Locate and identify every blood parasite.
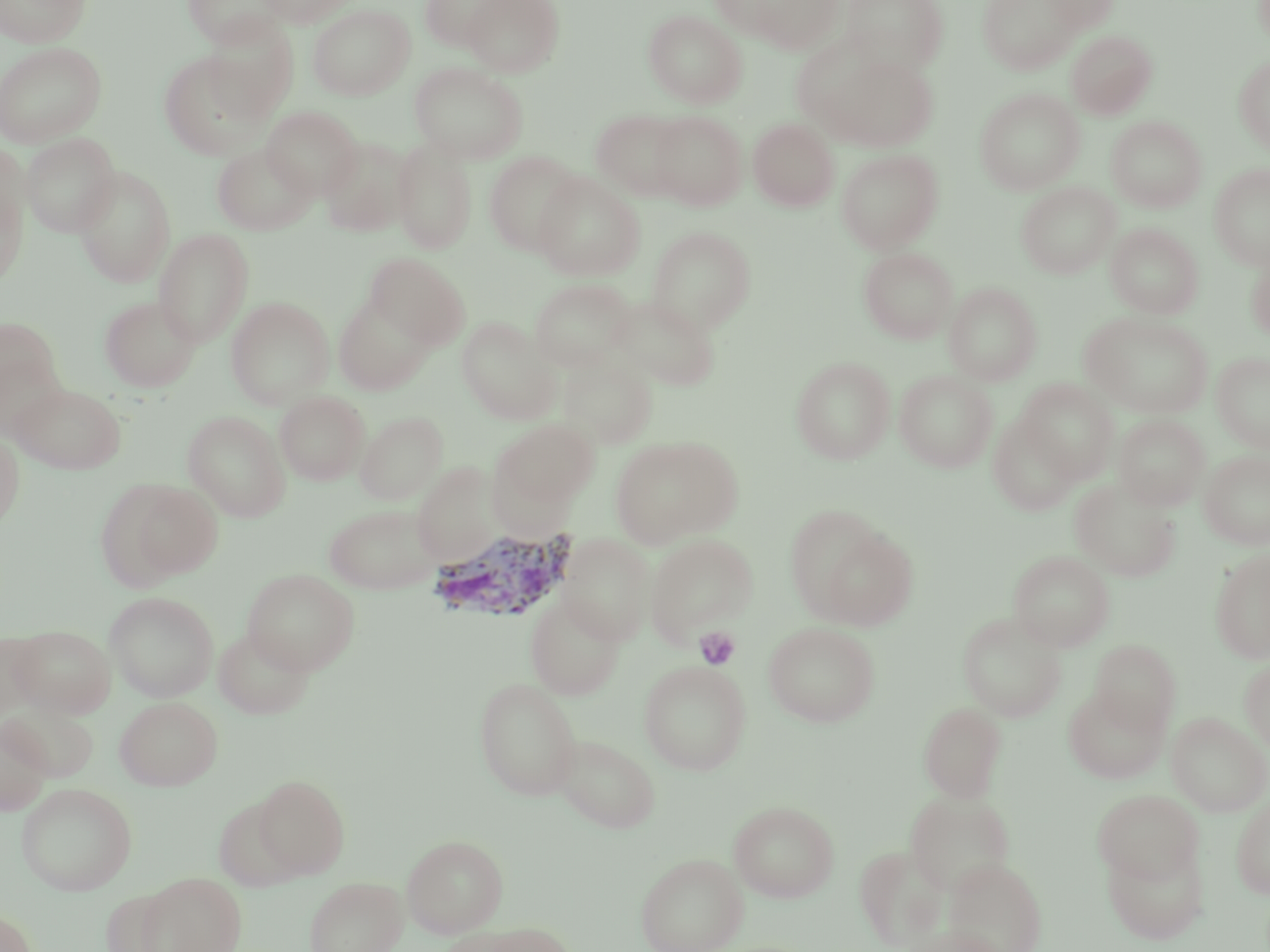

Approximate bounding boxes as named x1/y1/x2/y2 corners in pixels.
Plasmodium vivax-infected red blood cells: (x1=427, y1=528, x2=579, y2=624).
No Plasmodium falciparum, Plasmodium ovale, Plasmodium malariae, Babesia divergens, or Trypanosoma brucei observed.

Uninfected red blood cell locations: (x1=1, y1=0, x2=91, y2=47), (x1=182, y1=0, x2=286, y2=48), (x1=256, y1=0, x2=355, y2=27), (x1=418, y1=0, x2=515, y2=51), (x1=463, y1=0, x2=563, y2=77), (x1=710, y1=0, x2=811, y2=40), (x1=737, y1=0, x2=844, y2=52), (x1=841, y1=0, x2=948, y2=73), (x1=978, y1=0, x2=1082, y2=74), (x1=1043, y1=0, x2=1120, y2=34), (x1=2, y1=4, x2=100, y2=88), (x1=308, y1=4, x2=415, y2=100), (x1=643, y1=9, x2=746, y2=108), (x1=202, y1=18, x2=299, y2=120), (x1=1066, y1=30, x2=1157, y2=119), (x1=0, y1=42, x2=107, y2=148), (x1=158, y1=51, x2=269, y2=160), (x1=821, y1=52, x2=938, y2=151), (x1=1233, y1=55, x2=1270, y2=154), (x1=411, y1=62, x2=528, y2=162), (x1=975, y1=88, x2=1084, y2=194), (x1=262, y1=106, x2=362, y2=200), (x1=590, y1=109, x2=691, y2=200), (x1=650, y1=111, x2=747, y2=210), (x1=1106, y1=116, x2=1207, y2=212), (x1=748, y1=117, x2=839, y2=211), (x1=21, y1=133, x2=121, y2=236), (x1=319, y1=136, x2=414, y2=237), (x1=392, y1=139, x2=477, y2=255), (x1=0, y1=140, x2=28, y2=233), (x1=212, y1=143, x2=315, y2=235), (x1=836, y1=148, x2=944, y2=253), (x1=483, y1=151, x2=584, y2=257), (x1=1209, y1=163, x2=1270, y2=269), (x1=73, y1=166, x2=176, y2=287), (x1=533, y1=173, x2=644, y2=281), (x1=1016, y1=182, x2=1120, y2=279), (x1=0, y1=183, x2=27, y2=287), (x1=1105, y1=223, x2=1203, y2=319), (x1=646, y1=226, x2=756, y2=334), (x1=153, y1=228, x2=254, y2=348), (x1=858, y1=246, x2=958, y2=344), (x1=1245, y1=247, x2=1270, y2=343), (x1=366, y1=253, x2=469, y2=348), (x1=530, y1=278, x2=636, y2=371), (x1=944, y1=282, x2=1042, y2=385), (x1=333, y1=293, x2=436, y2=395), (x1=608, y1=294, x2=720, y2=391), (x1=99, y1=295, x2=201, y2=392), (x1=225, y1=296, x2=334, y2=409), (x1=1081, y1=312, x2=1213, y2=418), (x1=0, y1=315, x2=64, y2=415), (x1=457, y1=317, x2=560, y2=423), (x1=1211, y1=352, x2=1270, y2=452), (x1=557, y1=354, x2=658, y2=449), (x1=791, y1=356, x2=895, y2=463), (x1=895, y1=370, x2=997, y2=473), (x1=1017, y1=379, x2=1119, y2=483), (x1=10, y1=382, x2=126, y2=474), (x1=275, y1=390, x2=370, y2=485), (x1=183, y1=410, x2=290, y2=521), (x1=356, y1=411, x2=448, y2=504), (x1=988, y1=413, x2=1081, y2=516), (x1=1113, y1=414, x2=1210, y2=510), (x1=494, y1=419, x2=599, y2=508), (x1=0, y1=432, x2=24, y2=530), (x1=609, y1=435, x2=743, y2=548), (x1=1199, y1=449, x2=1270, y2=550), (x1=412, y1=462, x2=504, y2=567), (x1=1070, y1=478, x2=1181, y2=582), (x1=108, y1=479, x2=223, y2=584), (x1=323, y1=503, x2=443, y2=593), (x1=788, y1=512, x2=916, y2=630), (x1=557, y1=533, x2=656, y2=645), (x1=645, y1=534, x2=758, y2=644), (x1=1210, y1=548, x2=1270, y2=663), (x1=1008, y1=549, x2=1115, y2=651), (x1=243, y1=568, x2=359, y2=674), (x1=104, y1=591, x2=219, y2=701), (x1=525, y1=595, x2=625, y2=699), (x1=957, y1=612, x2=1067, y2=721), (x1=763, y1=622, x2=881, y2=727), (x1=10, y1=625, x2=116, y2=717), (x1=213, y1=626, x2=315, y2=720), (x1=0, y1=633, x2=43, y2=720), (x1=1089, y1=639, x2=1180, y2=732), (x1=1240, y1=658, x2=1270, y2=754), (x1=639, y1=660, x2=751, y2=775), (x1=474, y1=677, x2=582, y2=800), (x1=1063, y1=686, x2=1170, y2=784), (x1=115, y1=696, x2=222, y2=790), (x1=5, y1=701, x2=96, y2=785), (x1=918, y1=702, x2=1007, y2=802), (x1=1166, y1=712, x2=1270, y2=816), (x1=0, y1=718, x2=52, y2=815), (x1=552, y1=733, x2=661, y2=833), (x1=253, y1=775, x2=350, y2=879), (x1=15, y1=782, x2=137, y2=895), (x1=1093, y1=788, x2=1203, y2=885), (x1=904, y1=790, x2=1016, y2=896), (x1=1231, y1=796, x2=1270, y2=899), (x1=729, y1=800, x2=840, y2=903), (x1=402, y1=834, x2=509, y2=938), (x1=1101, y1=838, x2=1209, y2=943), (x1=855, y1=844, x2=949, y2=950), (x1=635, y1=852, x2=747, y2=952), (x1=945, y1=857, x2=1047, y2=952), (x1=134, y1=871, x2=247, y2=952), (x1=304, y1=876, x2=407, y2=952), (x1=0, y1=909, x2=37, y2=952), (x1=448, y1=921, x2=572, y2=952), (x1=904, y1=924, x2=1007, y2=952). Platelet locations: (x1=694, y1=627, x2=740, y2=670). Slide-level diagnosis: Plasmodium vivax. Image is 1270×952 pixels. Thin blood film. Optical microscopy. 1000x magnification. May-Grünwald-Giemsa-stained preparation. Single field of view.